Assess this cell for malaria.
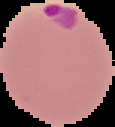

Parasitized.

Summary:
  - Preparation: thin blood smear
  - Image size: 115×127 pixels
  - Image type: segmented cell region with the area outside set to black